Name the cell type shown.
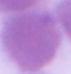

An erythrocyte.

modality: photomicrograph
magnification: 1000x